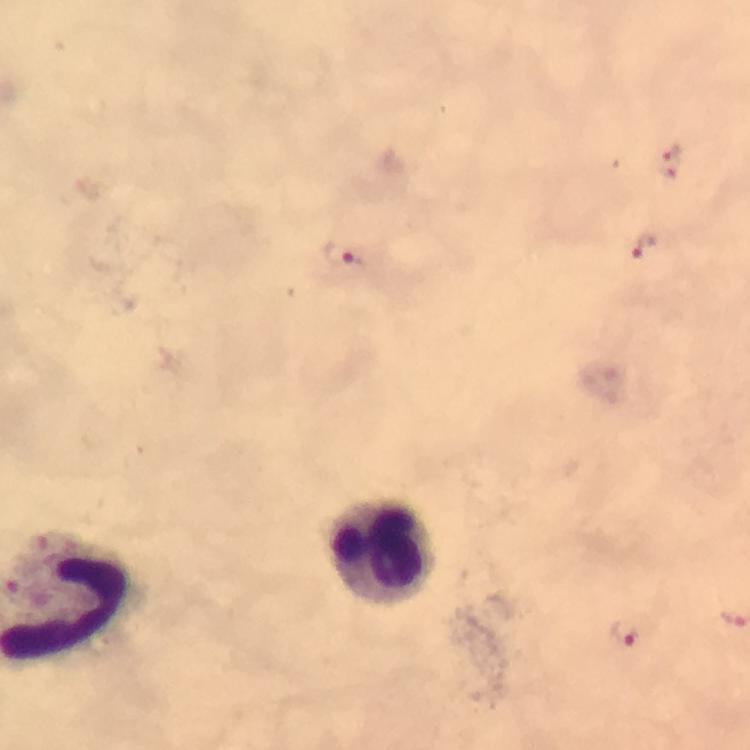
Approximate centers as [x, y] in pixels.
Summary:
  - Leukocyte locations: [384, 549]
  - Malaria parasite locations: [673, 161], [645, 245], [345, 255], [626, 631]
  - Magnification: 100x
  - Capture: smartphone mounted on the microscope
  - Stain: Giemsa
  - Preparation: thick blood film
  - Context: from a malaria diagnostic workup
  - Immersion oil: used
  - Image size: 750×750 pixels
  - Cropped from: a single field of view